Identify the parasite.
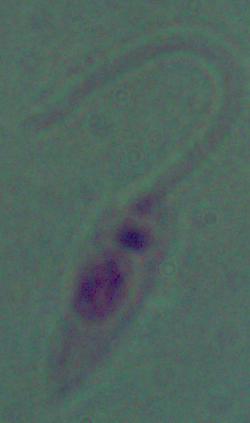
This is Leishmania.

modality: photomicrograph
magnification: 1000x